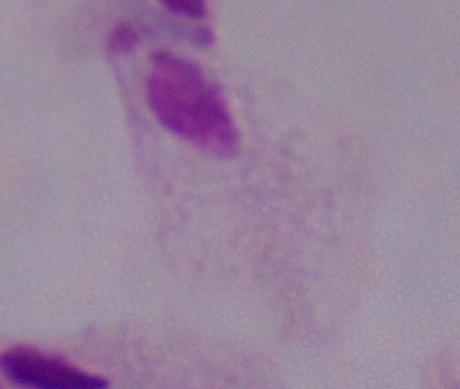
Summary:
  - Modality: photomicrograph
  - Identification: trichomonad
  - Magnification: 1000x